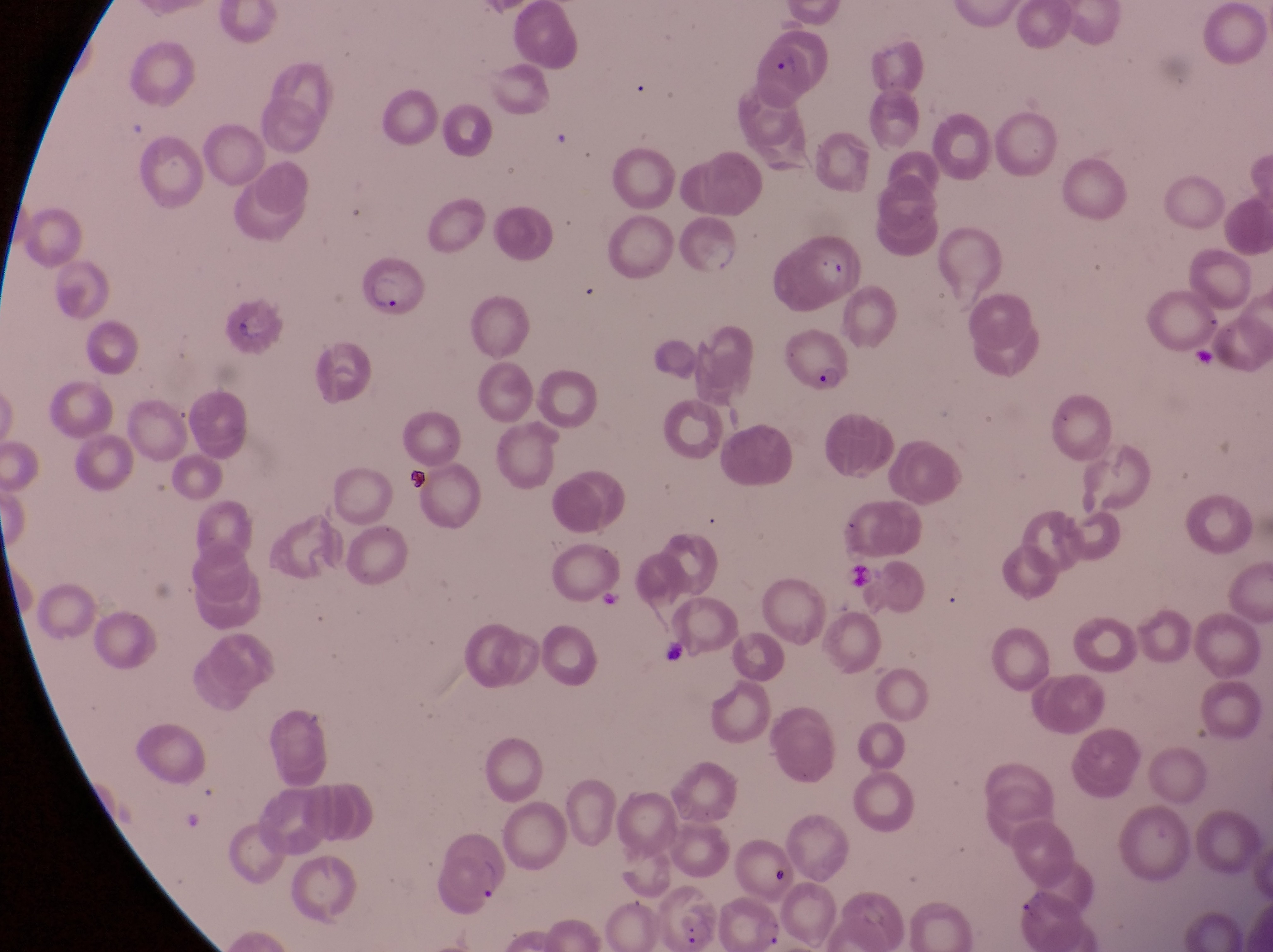
Approximate bounding boxes as {left, top, right, bottom} in pixels. Parasitised red blood cell locations: {757, 33, 834, 101}, {349, 264, 421, 314}, {784, 332, 853, 400}. Sample from Uganda. Captured by a smartphone held over the eyepiece of an Olympus CX-23 microscope. At a magnification of 1000x. Thin blood film. Image is 1273×952 pixels. Single field of view.